Assess the morphology of the red blood cells.
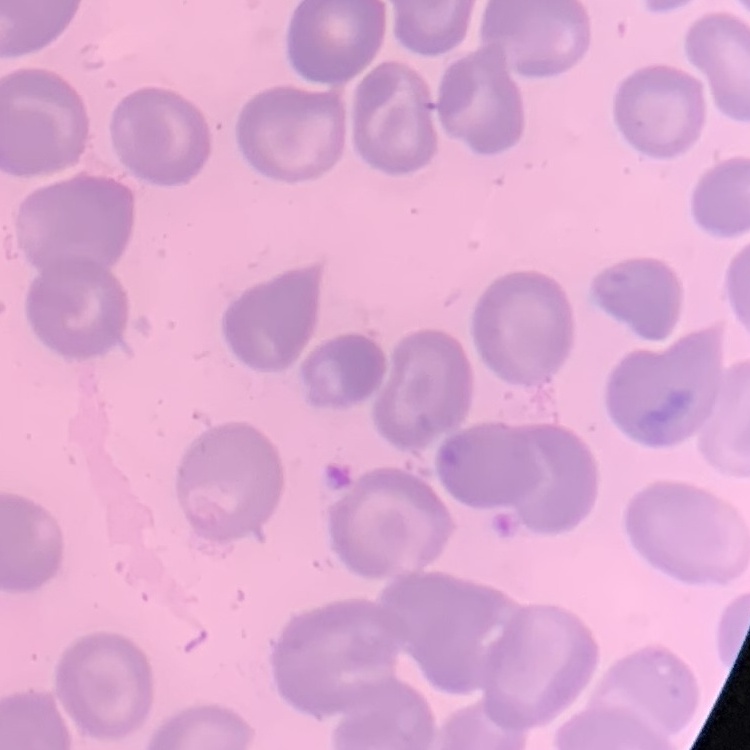

No rouleaux formation.

{
  "image_type": "one tile cut from a larger photomicrograph",
  "stain": "Field's or Giemsa",
  "preparation": "thin peripheral smear"
}